Locate every malaria parasite.
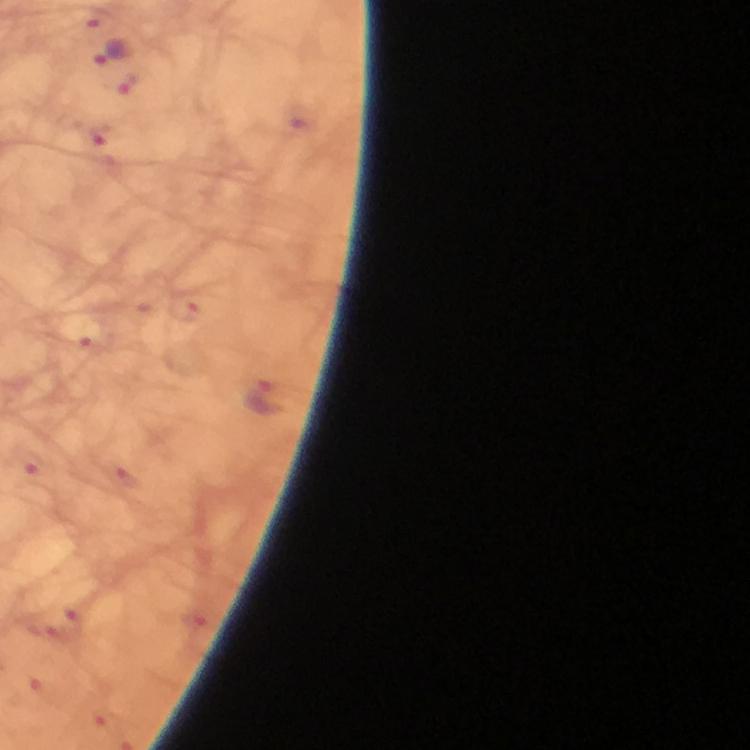

Approximate object centers, in pixels from the top-left corner.
Malaria parasites: (x=111, y=52), (x=132, y=83), (x=262, y=398).

Summary:
  - Capture: smartphone camera through the microscope
  - Magnification: 100x
  - Image size: 750×750 pixels
  - Context: from a diagnostic examination for malaria
  - Immersion oil: applied
  - Cropped from: a single field of view
  - Stain: Giemsa
  - Preparation: thick blood film